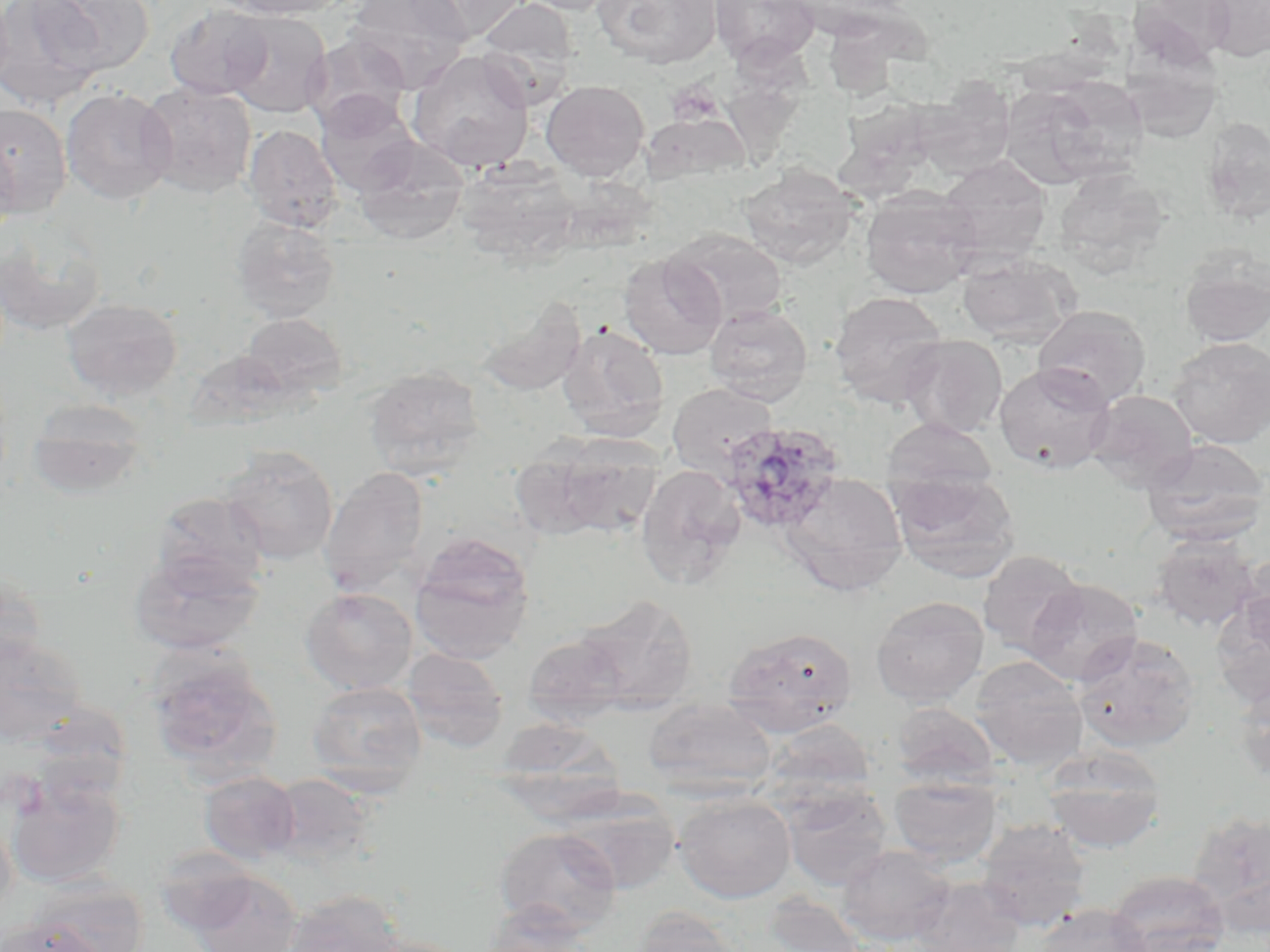

{
  "plasmodium_ovale_infected_red_blood_cell_locations": "approximate bounding boxes as [x1, y1, x2, y2] in pixels: [718, 420, 845, 534]",
  "slide_level_diagnosis": "Plasmodium ovale",
  "field_of_view": "single",
  "image_size": "1270×952 pixels",
  "preparation": "thin blood film",
  "uninfected_red_blood_cell_locations": "approximate bounding boxes as [x1, y1, x2, y2] in pixels: [0, 0, 15, 92], [1, 0, 104, 109], [33, 0, 156, 75], [216, 0, 346, 19], [344, 0, 471, 86], [408, 0, 526, 43], [475, 0, 580, 102], [514, 0, 622, 15], [593, 0, 723, 69], [710, 0, 819, 66], [1204, 0, 1270, 62], [1134, 1, 1233, 68], [165, 4, 274, 100], [223, 11, 332, 118], [303, 33, 415, 133], [407, 49, 535, 172], [916, 77, 1017, 181], [999, 77, 1140, 189], [541, 79, 650, 180], [136, 80, 257, 198], [60, 87, 176, 206], [315, 94, 420, 196], [0, 103, 72, 218], [261, 109, 393, 215], [643, 113, 748, 185], [1202, 118, 1270, 222], [243, 124, 343, 232], [0, 133, 19, 242], [353, 139, 470, 245], [937, 155, 1051, 262], [739, 165, 858, 270], [859, 188, 981, 299], [231, 216, 341, 323], [666, 229, 788, 326], [0, 230, 105, 336], [618, 251, 727, 359], [956, 253, 1080, 347], [1179, 256, 1270, 347], [971, 268, 1130, 373], [830, 291, 949, 408], [477, 296, 586, 396], [62, 298, 183, 399], [704, 303, 813, 405], [1032, 305, 1151, 408], [240, 312, 348, 399], [557, 324, 670, 439], [899, 335, 1008, 438], [1167, 337, 1270, 448], [183, 349, 296, 432], [993, 361, 1117, 475], [363, 366, 486, 476], [667, 382, 778, 479], [1086, 389, 1199, 493], [26, 398, 149, 499], [881, 417, 999, 505], [520, 435, 665, 541], [1140, 438, 1270, 544], [220, 445, 339, 564], [636, 464, 746, 588], [319, 466, 431, 593], [890, 471, 1020, 583], [780, 472, 908, 597], [151, 491, 269, 594], [409, 534, 535, 662], [1148, 534, 1261, 632], [128, 549, 263, 656], [977, 549, 1086, 657], [1239, 554, 1270, 661], [0, 566, 47, 676], [1023, 578, 1143, 687], [300, 587, 418, 695], [1214, 592, 1270, 709], [575, 594, 698, 712], [871, 596, 989, 706], [722, 627, 858, 736], [1, 632, 87, 747], [1073, 632, 1200, 754], [522, 633, 630, 724], [401, 648, 509, 752], [147, 653, 282, 783], [968, 656, 1089, 770], [1233, 675, 1270, 784], [306, 680, 427, 790], [642, 697, 778, 795], [890, 702, 999, 788], [492, 716, 623, 812], [762, 717, 877, 807], [1043, 746, 1166, 853], [5, 771, 127, 890], [199, 771, 300, 864], [265, 773, 380, 869], [888, 775, 1001, 867], [782, 786, 893, 891], [674, 793, 796, 903], [561, 798, 679, 894], [1185, 810, 1270, 925], [0, 811, 17, 926], [976, 818, 1091, 931], [494, 826, 623, 935], [837, 845, 955, 946], [153, 847, 261, 936], [187, 870, 302, 952], [1107, 870, 1229, 952], [909, 875, 1027, 952], [25, 877, 147, 951], [282, 888, 406, 952], [761, 893, 871, 951], [481, 904, 594, 952], [1035, 904, 1153, 952], [631, 906, 747, 952], [1, 917, 104, 952], [355, 936, 474, 952]",
  "platelet_locations": "approximate bounding boxes as [x1, y1, x2, y2] in pixels: [666, 81, 723, 125]",
  "modality": "light microscopy",
  "stain": "May-Grünwald-Giemsa",
  "magnification": "1000x"
}